Classify this cell by malaria status.
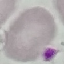
It is uninfected.

Summary:
  - Image type: automatically extracted cell patch, resized to 64 × 64 pixels
  - Stain: Giemsa
  - Preparation: thin smear
  - Capture: smartphone camera at the microscope eyepiece